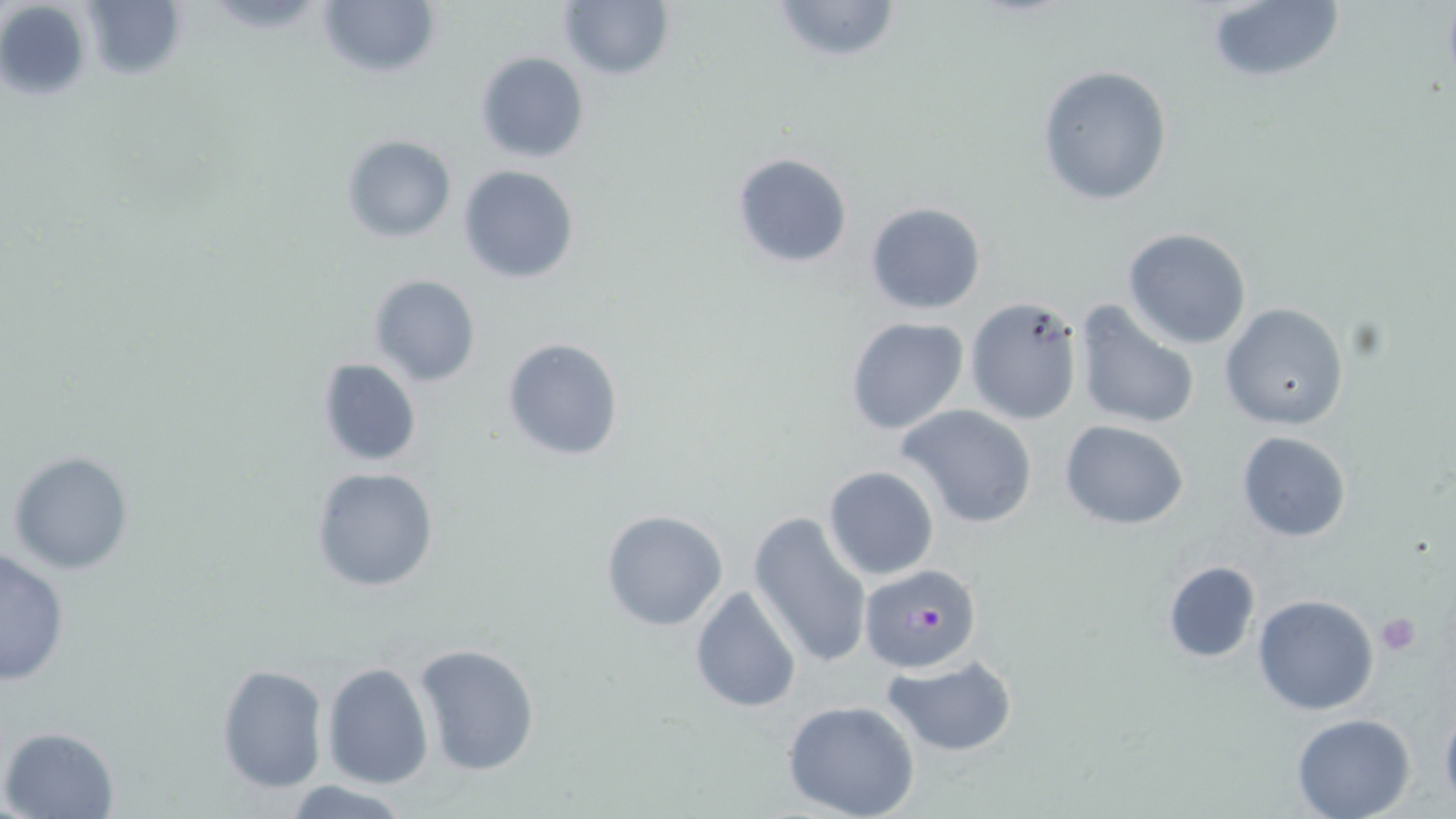
Approximate bounding boxes as (x1, y1, x2, y2) in pixels. Plasmodium falciparum-infected red blood cell locations: (859, 563, 984, 674). Uninfected red blood cell locations: (0, 0, 91, 104), (315, 0, 439, 82), (558, 0, 673, 80), (768, 0, 903, 64), (1204, 0, 1344, 88), (77, 1, 188, 83), (475, 52, 589, 163), (1036, 65, 1173, 205), (341, 134, 456, 242), (731, 152, 854, 268), (458, 165, 580, 283), (865, 202, 985, 314), (1123, 228, 1253, 349), (367, 273, 481, 389), (965, 296, 1086, 426), (1073, 300, 1202, 432), (1219, 303, 1349, 429), (844, 316, 971, 436), (501, 336, 626, 462), (315, 357, 422, 467), (897, 403, 1039, 529), (1059, 420, 1189, 530), (1236, 430, 1353, 541), (6, 451, 134, 575), (309, 465, 440, 593), (823, 466, 940, 581), (600, 509, 728, 630), (749, 511, 873, 669), (0, 548, 72, 687), (1161, 560, 1262, 662), (689, 585, 803, 714), (1252, 594, 1380, 715), (412, 641, 544, 778), (880, 655, 1020, 759), (321, 661, 433, 790), (215, 663, 328, 795), (1439, 698, 1456, 808), (783, 700, 921, 819), (1291, 710, 1416, 818), (3, 725, 119, 818), (281, 779, 415, 817). Platelet locations: (1375, 611, 1421, 655). Slide-level diagnosis: Plasmodium falciparum. Image is 1456×819 pixels. 1000x magnification. May-Grünwald-Giemsa-stained preparation. Thin blood film. Optical microscopy. One field of a larger specimen.